Assess this cell for malaria.
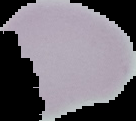
Uninfected.

The area outside the segmented cell region is set to black. From a thin blood smear. Image is 136×121 pixels.